Give the extent of all Plasmodium vivax-infected red blood cells.
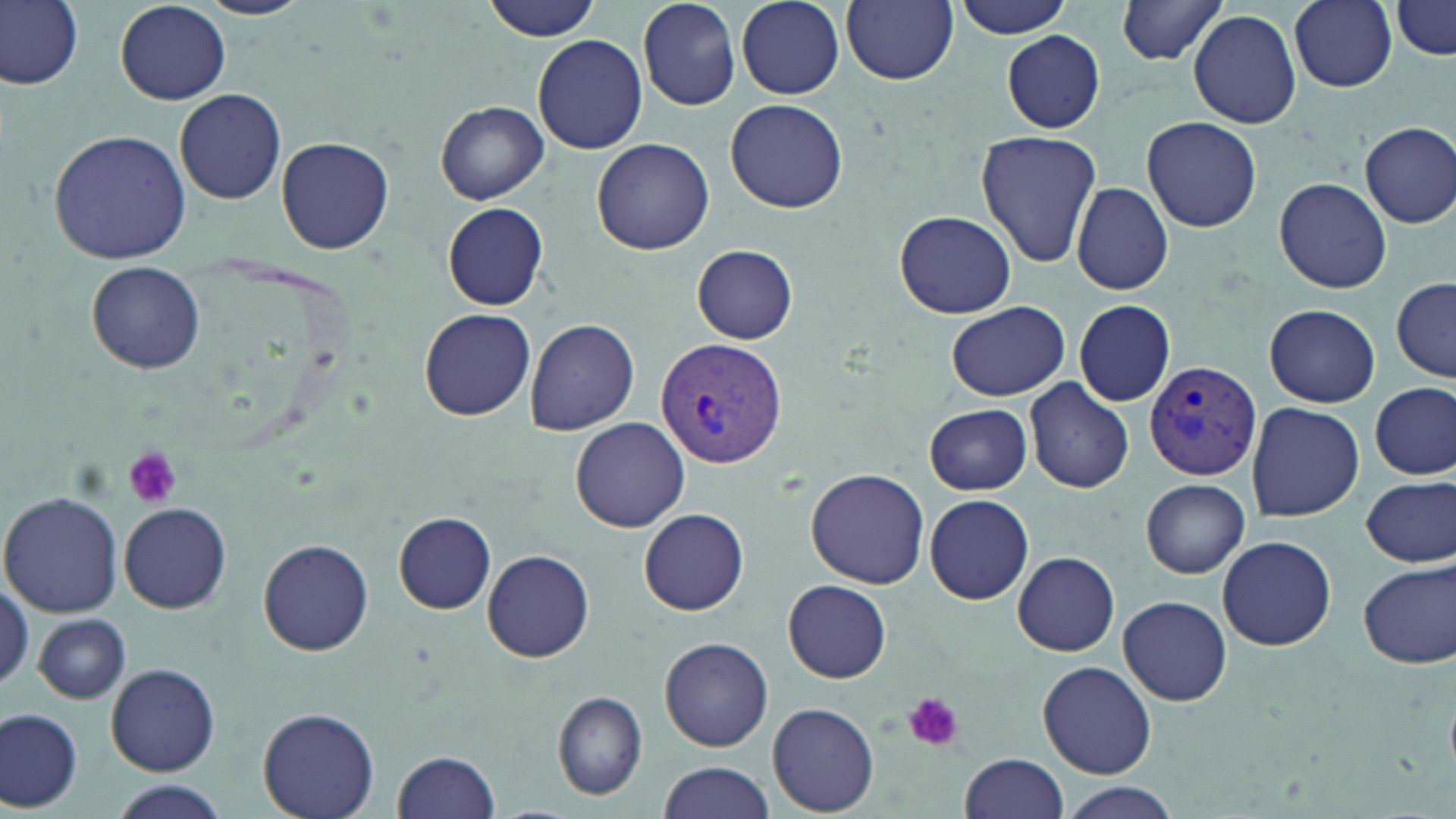

Approximate bounding boxes as named x1/y1/x2/y2 corners in pixels.
Plasmodium vivax-infected red blood cells: (x1=653, y1=335, x2=788, y2=469), (x1=1144, y1=360, x2=1263, y2=481).

slide-level diagnosis = Plasmodium vivax
uninfected red blood cell locations = approximate bounding boxes as named x1/y1/x2/y2 corners in pixels: (x1=1, y1=0, x2=84, y2=91), (x1=198, y1=0, x2=314, y2=19), (x1=481, y1=0, x2=601, y2=41), (x1=736, y1=0, x2=844, y2=98), (x1=950, y1=0, x2=1074, y2=39), (x1=1112, y1=0, x2=1233, y2=65), (x1=1289, y1=0, x2=1397, y2=91), (x1=115, y1=1, x2=231, y2=104), (x1=636, y1=1, x2=741, y2=111), (x1=842, y1=1, x2=957, y2=86), (x1=1390, y1=2, x2=1455, y2=60), (x1=1189, y1=8, x2=1302, y2=130), (x1=1000, y1=30, x2=1106, y2=132), (x1=534, y1=34, x2=648, y2=155), (x1=174, y1=88, x2=287, y2=204), (x1=726, y1=98, x2=847, y2=212), (x1=436, y1=102, x2=548, y2=204), (x1=1142, y1=116, x2=1262, y2=233), (x1=1359, y1=122, x2=1456, y2=227), (x1=48, y1=129, x2=190, y2=265), (x1=975, y1=131, x2=1101, y2=267), (x1=277, y1=138, x2=394, y2=254), (x1=592, y1=138, x2=715, y2=256), (x1=1275, y1=177, x2=1392, y2=294), (x1=1071, y1=181, x2=1173, y2=295), (x1=441, y1=202, x2=549, y2=310), (x1=894, y1=210, x2=1017, y2=318), (x1=692, y1=245, x2=799, y2=343), (x1=87, y1=261, x2=205, y2=372), (x1=1392, y1=278, x2=1455, y2=382), (x1=1074, y1=300, x2=1175, y2=407), (x1=947, y1=301, x2=1071, y2=400), (x1=1264, y1=304, x2=1380, y2=407), (x1=419, y1=309, x2=535, y2=421), (x1=524, y1=316, x2=641, y2=436), (x1=1024, y1=377, x2=1136, y2=494), (x1=1372, y1=382, x2=1454, y2=480), (x1=1246, y1=401, x2=1364, y2=522), (x1=925, y1=405, x2=1033, y2=495), (x1=570, y1=418, x2=689, y2=532), (x1=806, y1=468, x2=930, y2=588), (x1=1360, y1=475, x2=1455, y2=567), (x1=1142, y1=479, x2=1250, y2=577), (x1=1, y1=493, x2=123, y2=619), (x1=923, y1=494, x2=1033, y2=605), (x1=121, y1=501, x2=231, y2=613), (x1=639, y1=509, x2=750, y2=615), (x1=394, y1=512, x2=498, y2=613), (x1=1216, y1=536, x2=1337, y2=649), (x1=259, y1=538, x2=374, y2=656), (x1=483, y1=549, x2=594, y2=661), (x1=1012, y1=552, x2=1119, y2=655), (x1=1358, y1=559, x2=1455, y2=668), (x1=0, y1=574, x2=30, y2=695), (x1=783, y1=581, x2=892, y2=682), (x1=1119, y1=595, x2=1232, y2=706), (x1=33, y1=613, x2=130, y2=705), (x1=660, y1=636, x2=774, y2=752), (x1=1038, y1=661, x2=1157, y2=779), (x1=106, y1=663, x2=219, y2=775), (x1=553, y1=689, x2=648, y2=800), (x1=767, y1=702, x2=881, y2=815), (x1=258, y1=707, x2=380, y2=819), (x1=0, y1=708, x2=82, y2=812), (x1=392, y1=748, x2=500, y2=818), (x1=960, y1=753, x2=1068, y2=819), (x1=659, y1=760, x2=775, y2=818), (x1=109, y1=782, x2=230, y2=818), (x1=1059, y1=785, x2=1181, y2=819)
stain = May-Grünwald-Giemsa
modality = light microscopy
image size = 1456×819 pixels
magnification = 1000x
platelet locations = approximate bounding boxes as named x1/y1/x2/y2 corners in pixels: (x1=125, y1=447, x2=181, y2=508), (x1=903, y1=691, x2=963, y2=751)
preparation = thin blood film
field of view = one of a larger specimen